Point out each leukocyte.
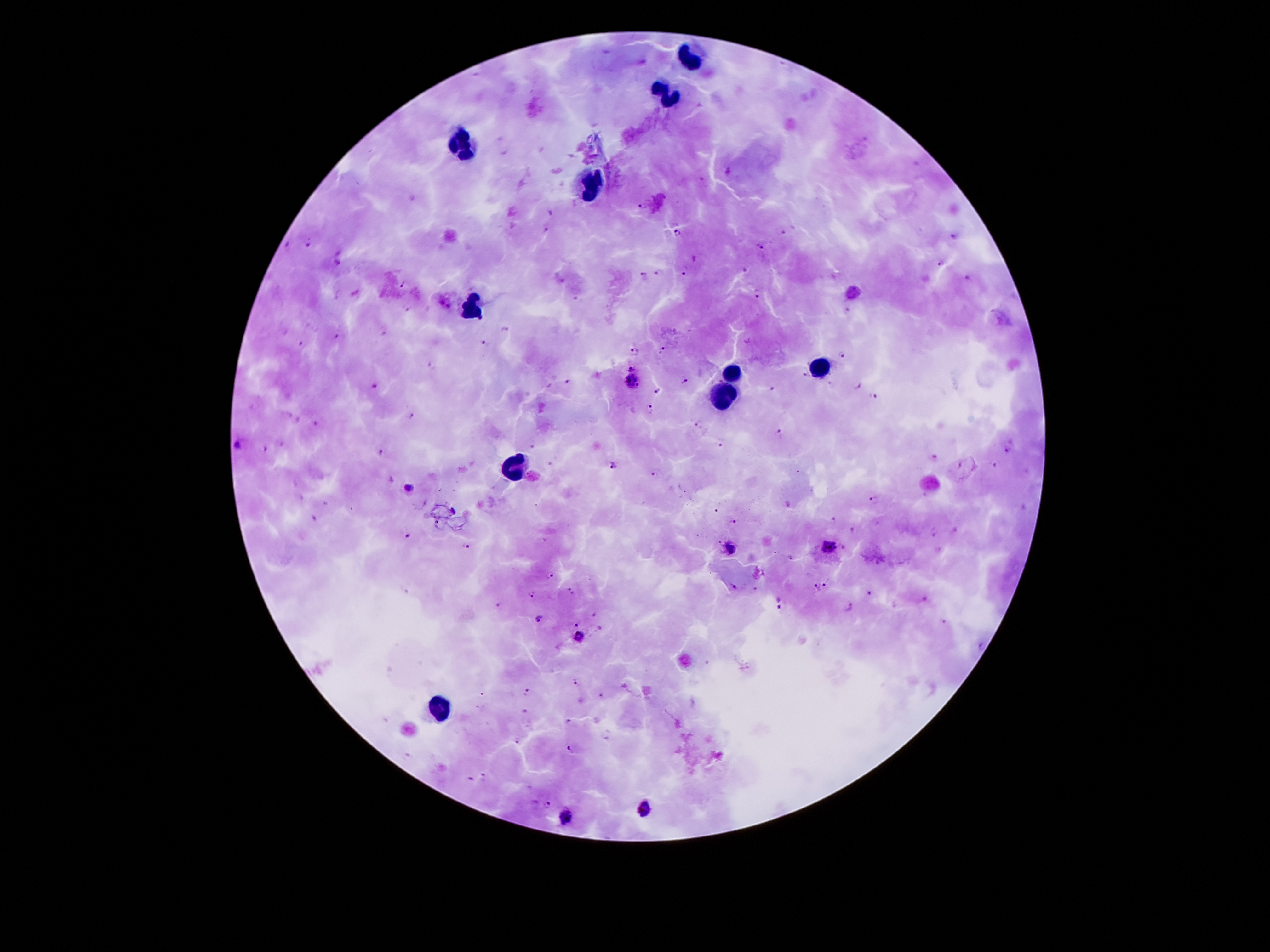
Approximate centers as (x, y) in pixels.
Leukocytes: (691, 58), (668, 94), (462, 142), (590, 186), (473, 306), (817, 367), (731, 375), (725, 396), (512, 469), (441, 705).

Summary:
  - Malaria parasite locations: (727, 173), (642, 204), (549, 213), (546, 230), (676, 232), (784, 233), (954, 237), (288, 245), (307, 245), (759, 246), (337, 263), (939, 263), (686, 269), (745, 269), (658, 273), (642, 276), (966, 279), (403, 282), (756, 295), (575, 298), (405, 307), (846, 313), (382, 328), (507, 329), (339, 335), (301, 344), (484, 344), (662, 349), (634, 352), (843, 354), (430, 364), (631, 368), (806, 374), (566, 380), (631, 381), (684, 381), (833, 384), (857, 384), (374, 386), (770, 390), (655, 391), (873, 396), (650, 407), (412, 415), (316, 424), (696, 426), (779, 434), (280, 443), (721, 443), (239, 444), (265, 451), (379, 451), (1009, 451), (934, 459), (995, 464), (613, 465), (653, 473), (407, 488), (876, 500), (715, 510), (314, 517), (734, 519), (833, 521), (853, 531), (407, 533), (935, 533), (466, 546), (828, 546), (733, 549), (550, 572), (828, 583), (732, 584), (757, 586), (405, 589), (816, 589), (572, 590), (532, 593), (869, 593), (925, 599), (779, 601), (498, 604), (895, 604), (847, 607), (599, 611), (541, 618), (576, 621), (944, 624), (599, 629), (579, 635), (579, 682), (526, 690), (603, 695), (526, 712), (569, 722), (518, 739), (572, 748), (470, 778), (483, 778), (548, 805), (645, 807), (567, 818)
  - Preparation: thick blood smear
  - Image size: 1270×952 pixels
  - Patient malaria status: infected with Plasmodium falciparum
  - Magnification: 100x
  - Field of view: single
  - Capture: smartphone through the microscope eyepiece
  - Stain: Giemsa